Outline each blood parasite and name the species.
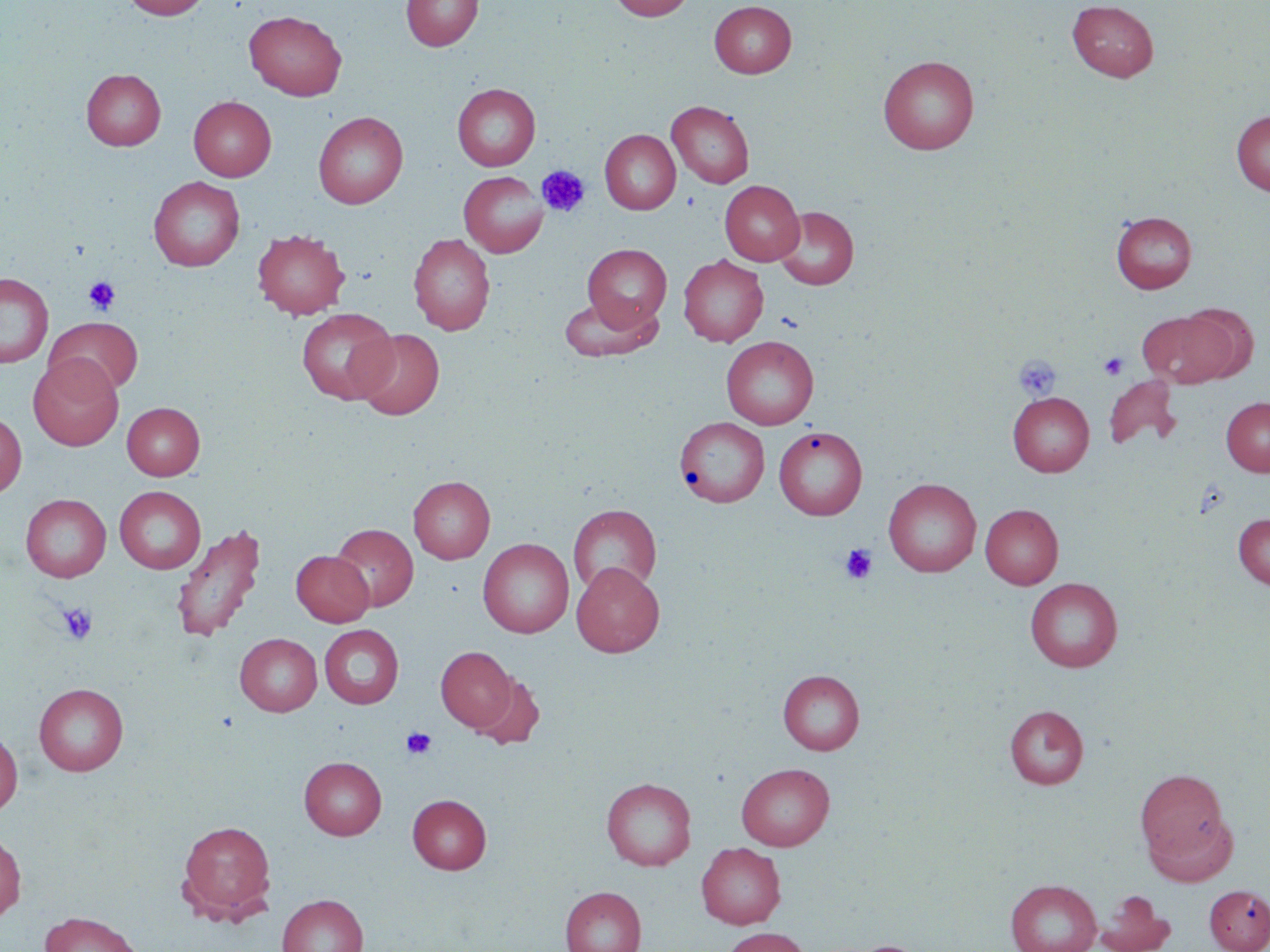

No blood parasites observed.

Approximate bounding boxes as named x1/y1/x2/y2 corners in pixels. Platelet locations: (x1=537, y1=165, x2=590, y2=218), (x1=83, y1=276, x2=121, y2=315), (x1=1098, y1=352, x2=1129, y2=380), (x1=1014, y1=355, x2=1060, y2=400), (x1=840, y1=544, x2=877, y2=584), (x1=58, y1=602, x2=98, y2=645), (x1=401, y1=727, x2=437, y2=759). Uninfected red blood cell locations: (x1=121, y1=0, x2=211, y2=19), (x1=401, y1=0, x2=483, y2=51), (x1=609, y1=0, x2=695, y2=21), (x1=709, y1=1, x2=797, y2=78), (x1=1067, y1=1, x2=1158, y2=81), (x1=244, y1=10, x2=347, y2=100), (x1=878, y1=55, x2=980, y2=154), (x1=81, y1=68, x2=166, y2=150), (x1=452, y1=83, x2=540, y2=171), (x1=189, y1=96, x2=276, y2=181), (x1=667, y1=100, x2=754, y2=189), (x1=1231, y1=110, x2=1270, y2=196), (x1=313, y1=111, x2=408, y2=209), (x1=599, y1=129, x2=680, y2=215), (x1=458, y1=171, x2=548, y2=257), (x1=148, y1=176, x2=245, y2=271), (x1=720, y1=179, x2=804, y2=265), (x1=773, y1=206, x2=859, y2=290), (x1=1111, y1=210, x2=1197, y2=293), (x1=252, y1=229, x2=350, y2=319), (x1=408, y1=233, x2=495, y2=335), (x1=582, y1=244, x2=672, y2=330), (x1=678, y1=255, x2=768, y2=346), (x1=0, y1=272, x2=53, y2=368), (x1=558, y1=295, x2=662, y2=362), (x1=1175, y1=303, x2=1259, y2=382), (x1=296, y1=308, x2=398, y2=404), (x1=1137, y1=309, x2=1236, y2=388), (x1=45, y1=317, x2=143, y2=396), (x1=353, y1=328, x2=444, y2=419), (x1=721, y1=336, x2=819, y2=429), (x1=29, y1=356, x2=123, y2=451), (x1=1104, y1=374, x2=1181, y2=451), (x1=1008, y1=392, x2=1094, y2=476), (x1=1221, y1=397, x2=1270, y2=476), (x1=122, y1=402, x2=205, y2=480), (x1=0, y1=412, x2=26, y2=498), (x1=675, y1=416, x2=769, y2=507), (x1=773, y1=426, x2=867, y2=520), (x1=409, y1=475, x2=495, y2=564), (x1=883, y1=478, x2=981, y2=577), (x1=114, y1=486, x2=206, y2=573), (x1=21, y1=494, x2=111, y2=582), (x1=568, y1=504, x2=662, y2=597), (x1=980, y1=504, x2=1063, y2=589), (x1=1233, y1=514, x2=1270, y2=589), (x1=171, y1=523, x2=266, y2=643), (x1=331, y1=523, x2=418, y2=611), (x1=478, y1=538, x2=574, y2=637), (x1=291, y1=550, x2=374, y2=626), (x1=572, y1=562, x2=664, y2=657), (x1=1025, y1=578, x2=1123, y2=672), (x1=319, y1=625, x2=404, y2=708), (x1=235, y1=633, x2=322, y2=716), (x1=436, y1=646, x2=516, y2=731), (x1=778, y1=670, x2=865, y2=755), (x1=471, y1=672, x2=545, y2=749), (x1=34, y1=683, x2=129, y2=776), (x1=1005, y1=705, x2=1089, y2=788), (x1=0, y1=727, x2=22, y2=817), (x1=299, y1=756, x2=386, y2=840), (x1=736, y1=763, x2=834, y2=850), (x1=1136, y1=769, x2=1228, y2=861), (x1=601, y1=777, x2=696, y2=870), (x1=408, y1=794, x2=491, y2=874), (x1=1146, y1=813, x2=1238, y2=886), (x1=177, y1=820, x2=276, y2=921), (x1=0, y1=830, x2=26, y2=922), (x1=696, y1=842, x2=786, y2=929), (x1=1005, y1=879, x2=1102, y2=952), (x1=1204, y1=884, x2=1270, y2=952), (x1=560, y1=886, x2=646, y2=952), (x1=1096, y1=890, x2=1176, y2=952), (x1=278, y1=894, x2=367, y2=952), (x1=38, y1=911, x2=144, y2=952), (x1=721, y1=927, x2=811, y2=952), (x1=834, y1=940, x2=935, y2=952). Slide-level diagnosis: no evidence of blood parasites. Optical microscopy. May-Grünwald-Giemsa stain. Single field of view. Captured at 1000x magnification. Thin blood smear. Image is 1270×952 pixels.